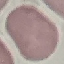

Summary:
  - Malaria status: uninfected
  - Preparation: thin smear
  - Stain: Giemsa
  - Capture: smartphone camera at the microscope eyepiece
  - Image type: automatically extracted cell patch, resized to 64 × 64 pixels